Assess this cell for malaria.
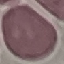

Uninfected.

{
  "preparation": "thin blood smear",
  "image_type": "cell patch, automatically extracted from a larger field of view and resized to 64 × 64 pixels",
  "capture": "smartphone through the microscope eyepiece",
  "stain": "Giemsa"
}